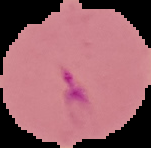 Image is 151×148 pixels. From a thin blood film. Cell region segmented out of the field of view; the surrounding area is masked to black. Malaria status: parasitized.